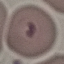
Summary:
  - Result: malaria parasites detected
  - Preparation: thin blood film
  - Image type: cell patch, automatically extracted from a larger field of view and resized to 64 × 64 pixels
  - Stain: Giemsa
  - Capture: smartphone camera at the microscope eyepiece